Report the malaria status of this cell.
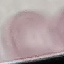
It is uninfected.

image type = cell patch, automatically extracted from a larger field of view and resized to 64 × 64 pixels
capture = smartphone camera at the microscope eyepiece
preparation = thin blood film
stain = Giemsa